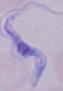
Captured at 1000x magnification. A trypanosome is shown. Micrograph.